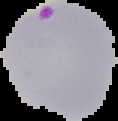
Summary:
  - Image size: 118×121 pixels
  - Preparation: thin blood film
  - Malaria status: parasitized
  - Image type: segmented cell region with the area outside set to black